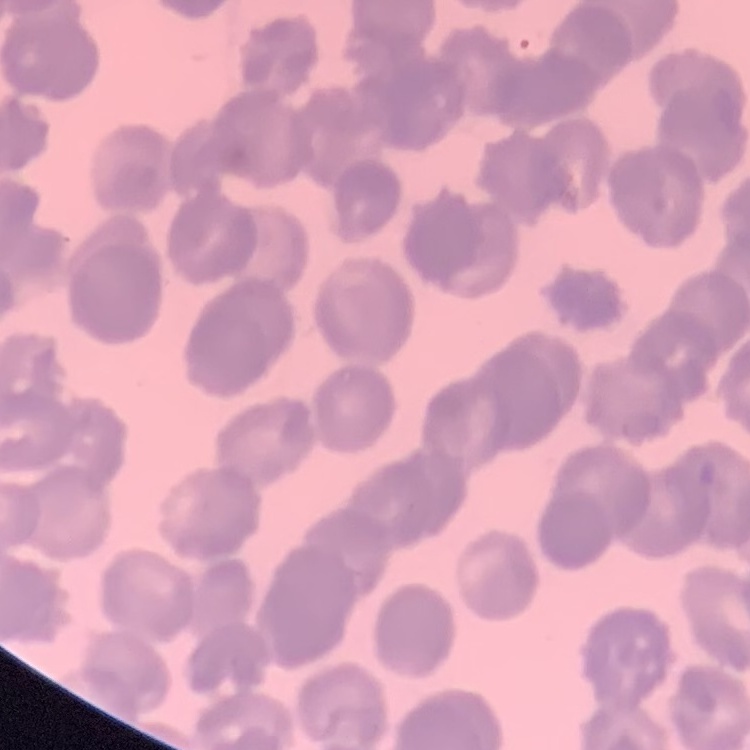

The red blood cells exhibit rouleaux formation. Field's or Giemsa stain. Thin blood film. One tile cut from a larger photomicrograph.